Name the blood parasite species.
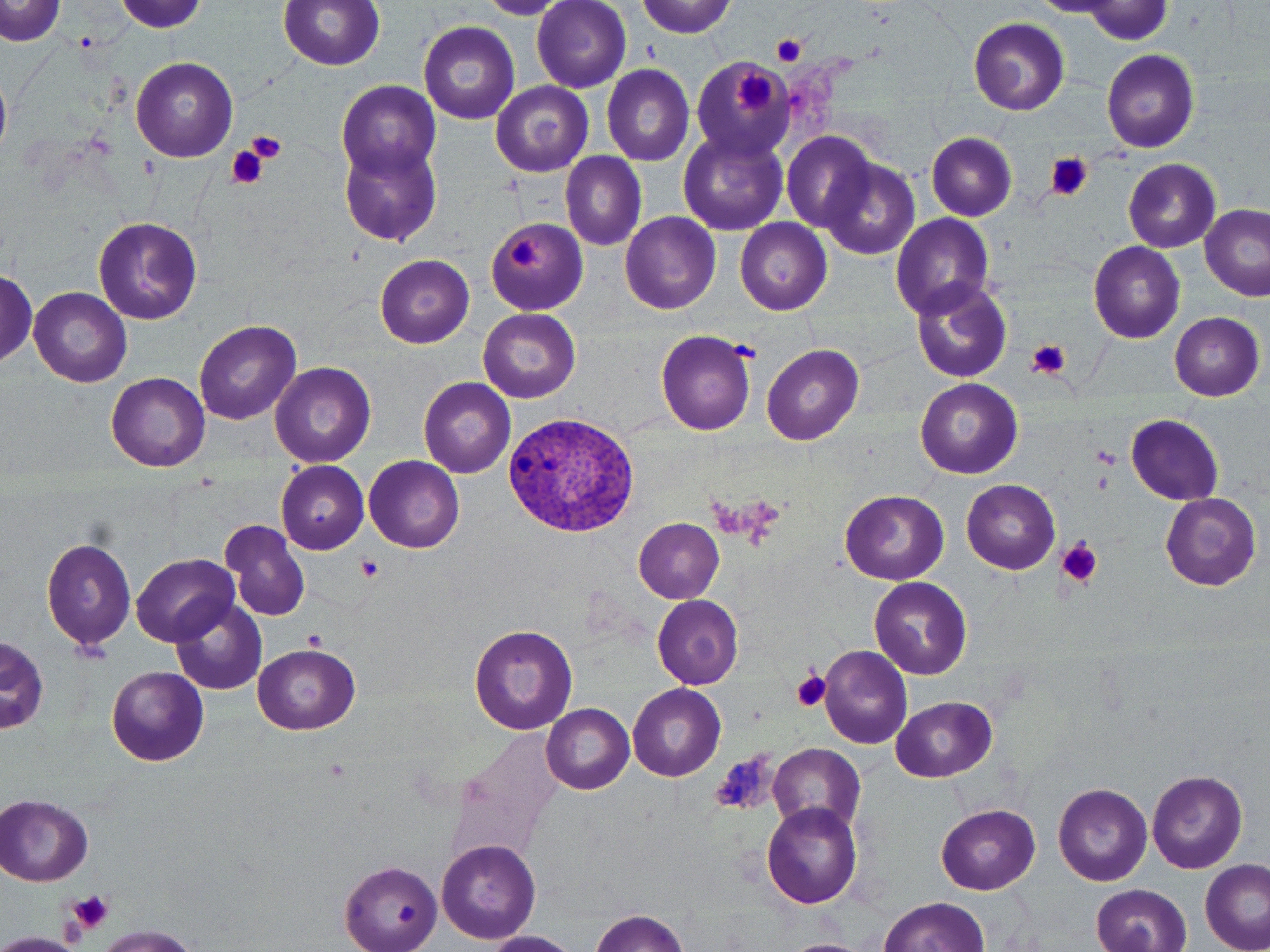
Plasmodium vivax.

preparation = thin blood film
image size = 1270×952 pixels
field of view = one of a larger specimen
stain = May-Grünwald-Giemsa
modality = optical microscopy
magnification = 1000x
Plasmodium vivax-infected red blood cell locations = approximate bounding boxes as named x1/y1/x2/y2 corners in pixels: (x1=502, y1=409, x2=645, y2=539)
uninfected red blood cell locations = approximate bounding boxes as named x1/y1/x2/y2 corners in pixels: (x1=278, y1=0, x2=384, y2=70), (x1=0, y1=1, x2=66, y2=46), (x1=117, y1=1, x2=206, y2=32), (x1=533, y1=1, x2=631, y2=94), (x1=636, y1=1, x2=735, y2=37), (x1=968, y1=17, x2=1069, y2=116), (x1=419, y1=20, x2=518, y2=124), (x1=1100, y1=49, x2=1199, y2=153), (x1=131, y1=56, x2=238, y2=162), (x1=688, y1=56, x2=791, y2=158), (x1=602, y1=64, x2=695, y2=165), (x1=0, y1=77, x2=12, y2=157), (x1=336, y1=81, x2=442, y2=185), (x1=490, y1=82, x2=593, y2=178), (x1=678, y1=129, x2=789, y2=236), (x1=782, y1=132, x2=878, y2=235), (x1=927, y1=133, x2=1016, y2=220), (x1=339, y1=142, x2=441, y2=245), (x1=562, y1=153, x2=647, y2=251), (x1=818, y1=157, x2=920, y2=260), (x1=1124, y1=159, x2=1220, y2=253), (x1=1200, y1=205, x2=1269, y2=301), (x1=620, y1=212, x2=721, y2=314), (x1=891, y1=213, x2=994, y2=317), (x1=93, y1=216, x2=202, y2=325), (x1=486, y1=218, x2=587, y2=314), (x1=735, y1=218, x2=832, y2=316), (x1=1088, y1=241, x2=1185, y2=343), (x1=375, y1=254, x2=474, y2=348), (x1=0, y1=272, x2=39, y2=364), (x1=909, y1=276, x2=1012, y2=383), (x1=30, y1=287, x2=132, y2=388), (x1=479, y1=308, x2=581, y2=404), (x1=1169, y1=312, x2=1264, y2=400), (x1=195, y1=320, x2=300, y2=424), (x1=654, y1=328, x2=758, y2=436), (x1=763, y1=343, x2=864, y2=445), (x1=271, y1=361, x2=376, y2=469), (x1=106, y1=373, x2=209, y2=471), (x1=418, y1=377, x2=516, y2=477), (x1=916, y1=378, x2=1022, y2=478), (x1=1127, y1=414, x2=1223, y2=506), (x1=363, y1=455, x2=464, y2=553), (x1=276, y1=460, x2=369, y2=555), (x1=962, y1=479, x2=1061, y2=574), (x1=840, y1=490, x2=949, y2=584), (x1=1158, y1=491, x2=1261, y2=590), (x1=634, y1=518, x2=724, y2=603), (x1=219, y1=519, x2=311, y2=621), (x1=42, y1=536, x2=136, y2=652), (x1=133, y1=553, x2=239, y2=645), (x1=869, y1=576, x2=972, y2=679), (x1=651, y1=594, x2=745, y2=689), (x1=173, y1=600, x2=267, y2=695), (x1=470, y1=624, x2=578, y2=735), (x1=2, y1=637, x2=48, y2=735), (x1=253, y1=643, x2=360, y2=734), (x1=819, y1=646, x2=913, y2=749), (x1=107, y1=666, x2=209, y2=766), (x1=627, y1=683, x2=726, y2=781), (x1=893, y1=696, x2=998, y2=782), (x1=542, y1=704, x2=634, y2=794), (x1=769, y1=746, x2=863, y2=830), (x1=1147, y1=770, x2=1249, y2=874), (x1=1054, y1=783, x2=1152, y2=886), (x1=0, y1=795, x2=93, y2=886), (x1=761, y1=802, x2=864, y2=911), (x1=936, y1=803, x2=1040, y2=894), (x1=437, y1=840, x2=541, y2=944), (x1=340, y1=862, x2=442, y2=952), (x1=1201, y1=862, x2=1270, y2=951), (x1=1090, y1=883, x2=1191, y2=952), (x1=878, y1=898, x2=989, y2=951), (x1=591, y1=909, x2=691, y2=951), (x1=93, y1=924, x2=197, y2=952), (x1=480, y1=932, x2=578, y2=952), (x1=788, y1=939, x2=865, y2=952)
platelet locations = approximate bounding boxes as named x1/y1/x2/y2 corners in pixels: (x1=771, y1=36, x2=807, y2=68), (x1=735, y1=70, x2=774, y2=116), (x1=245, y1=131, x2=286, y2=163), (x1=228, y1=146, x2=268, y2=188), (x1=1046, y1=153, x2=1092, y2=200), (x1=509, y1=236, x2=543, y2=271), (x1=1026, y1=339, x2=1073, y2=379), (x1=1094, y1=447, x2=1119, y2=467), (x1=1094, y1=473, x2=1112, y2=492), (x1=1057, y1=538, x2=1104, y2=587), (x1=356, y1=553, x2=384, y2=581), (x1=304, y1=630, x2=326, y2=650), (x1=792, y1=670, x2=832, y2=712), (x1=713, y1=752, x2=776, y2=816), (x1=70, y1=890, x2=113, y2=931)